Identify the blood parasite species.
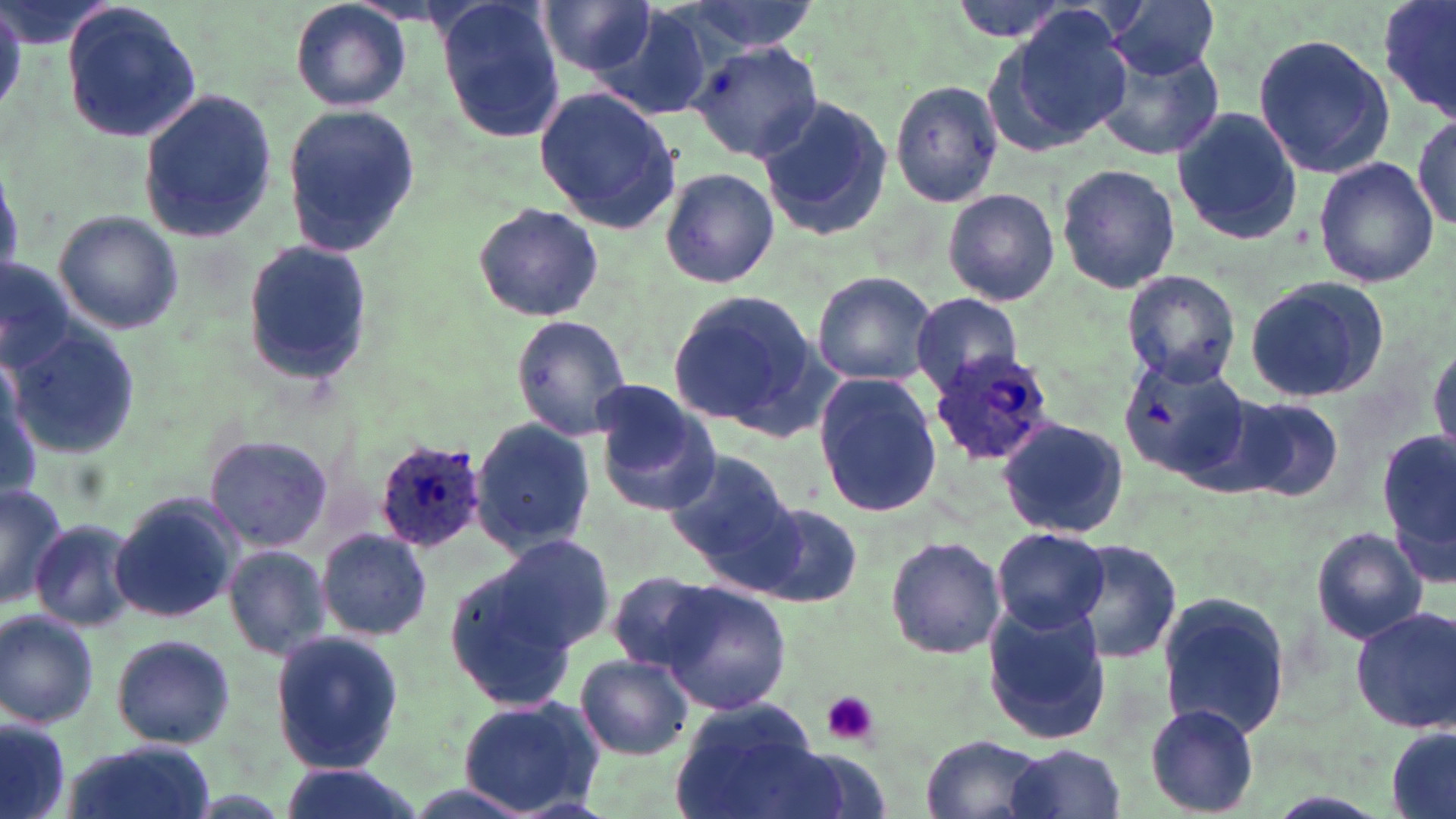
Plasmodium ovale.

Approximate bounding boxes as named x1/y1/x2/y2 corners in pixels. Plasmodium ovale-infected red blood cell locations: (x1=928, y1=352, x2=1055, y2=467), (x1=369, y1=435, x2=490, y2=555). Uninfected red blood cell locations: (x1=290, y1=0, x2=411, y2=112), (x1=538, y1=0, x2=661, y2=77), (x1=667, y1=0, x2=821, y2=56), (x1=947, y1=0, x2=1085, y2=44), (x1=1104, y1=0, x2=1223, y2=77), (x1=1376, y1=0, x2=1455, y2=118), (x1=61, y1=1, x2=202, y2=145), (x1=435, y1=3, x2=569, y2=141), (x1=601, y1=3, x2=720, y2=120), (x1=986, y1=11, x2=1136, y2=152), (x1=1253, y1=34, x2=1395, y2=179), (x1=688, y1=41, x2=823, y2=164), (x1=1090, y1=41, x2=1226, y2=161), (x1=890, y1=79, x2=1006, y2=209), (x1=534, y1=86, x2=680, y2=235), (x1=138, y1=87, x2=279, y2=241), (x1=756, y1=95, x2=892, y2=243), (x1=282, y1=103, x2=420, y2=257), (x1=1172, y1=108, x2=1305, y2=244), (x1=1410, y1=109, x2=1456, y2=236), (x1=1312, y1=156, x2=1438, y2=287), (x1=1056, y1=162, x2=1179, y2=294), (x1=659, y1=167, x2=778, y2=288), (x1=942, y1=187, x2=1061, y2=307), (x1=472, y1=203, x2=603, y2=322), (x1=55, y1=213, x2=181, y2=333), (x1=242, y1=240, x2=372, y2=388), (x1=1, y1=256, x2=75, y2=374), (x1=1121, y1=269, x2=1241, y2=388), (x1=810, y1=271, x2=937, y2=387), (x1=1242, y1=276, x2=1390, y2=402), (x1=666, y1=290, x2=820, y2=434), (x1=910, y1=294, x2=1026, y2=392), (x1=513, y1=316, x2=632, y2=439), (x1=11, y1=335, x2=137, y2=460), (x1=1429, y1=343, x2=1456, y2=459), (x1=1122, y1=356, x2=1255, y2=486), (x1=812, y1=373, x2=944, y2=517), (x1=1, y1=384, x2=44, y2=503), (x1=591, y1=385, x2=720, y2=514), (x1=1227, y1=396, x2=1343, y2=503), (x1=996, y1=416, x2=1129, y2=538), (x1=471, y1=418, x2=594, y2=557), (x1=1384, y1=430, x2=1456, y2=577), (x1=204, y1=435, x2=334, y2=551), (x1=661, y1=448, x2=800, y2=572), (x1=0, y1=483, x2=69, y2=609), (x1=110, y1=492, x2=240, y2=626), (x1=753, y1=504, x2=864, y2=608), (x1=27, y1=517, x2=143, y2=636), (x1=991, y1=525, x2=1109, y2=635), (x1=1311, y1=526, x2=1427, y2=644), (x1=315, y1=528, x2=433, y2=642), (x1=883, y1=533, x2=1006, y2=659), (x1=495, y1=534, x2=615, y2=653), (x1=1060, y1=538, x2=1183, y2=663), (x1=224, y1=546, x2=332, y2=659), (x1=443, y1=563, x2=584, y2=712), (x1=607, y1=570, x2=725, y2=675), (x1=655, y1=581, x2=791, y2=716), (x1=1157, y1=592, x2=1290, y2=739), (x1=981, y1=602, x2=1113, y2=747), (x1=1351, y1=608, x2=1456, y2=734), (x1=0, y1=610, x2=100, y2=729), (x1=268, y1=629, x2=404, y2=773), (x1=106, y1=632, x2=236, y2=750), (x1=575, y1=653, x2=695, y2=760), (x1=456, y1=694, x2=605, y2=816), (x1=670, y1=700, x2=828, y2=819), (x1=1145, y1=704, x2=1259, y2=817), (x1=0, y1=715, x2=73, y2=819), (x1=1386, y1=724, x2=1456, y2=817), (x1=918, y1=734, x2=1050, y2=819), (x1=58, y1=742, x2=218, y2=819), (x1=999, y1=744, x2=1128, y2=819), (x1=271, y1=762, x2=431, y2=819). Platelet locations: (x1=819, y1=690, x2=879, y2=746). Thin blood film. Captured at 1000x magnification. One field of a larger specimen. Image is 1456×819 pixels. May-Grünwald-Giemsa stain. Light microscopy.